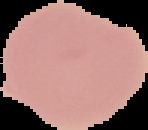

result = no Plasmodium parasites detected
image size = 148×130 pixels
image type = segmented cell region with the area outside set to black
preparation = thin blood smear